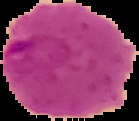
Result: malaria parasites identified. Image is 139×121 pixels. From a thin blood smear. The area outside the segmented cell region is set to black.